Assess for malaria.
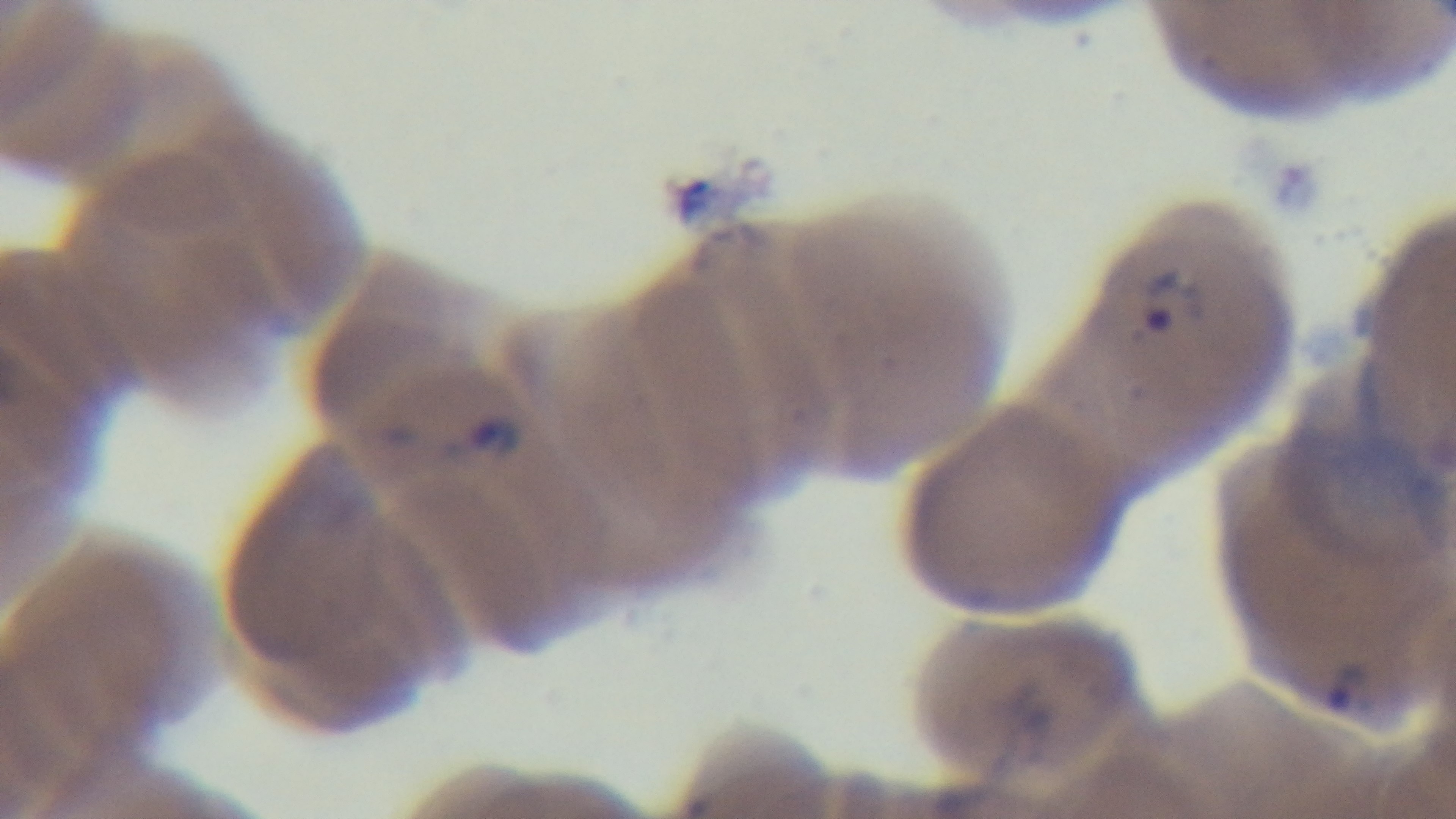
Positive.

Summary:
  - Objective: 100x oil immersion
  - Preparation: thin smear
  - Capture: mounted 4K digital camera
  - Field of view: one from the slide
  - Modality: light microscopy
  - Stain: Giemsa